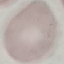
Summary:
  - Malaria status: uninfected
  - Capture: smartphone through the microscope eyepiece
  - Stain: Giemsa
  - Preparation: thin smear
  - Image type: cell patch, automatically extracted from a larger field of view and resized to 64 × 64 pixels